Give the position of every Plasmodium parasite.
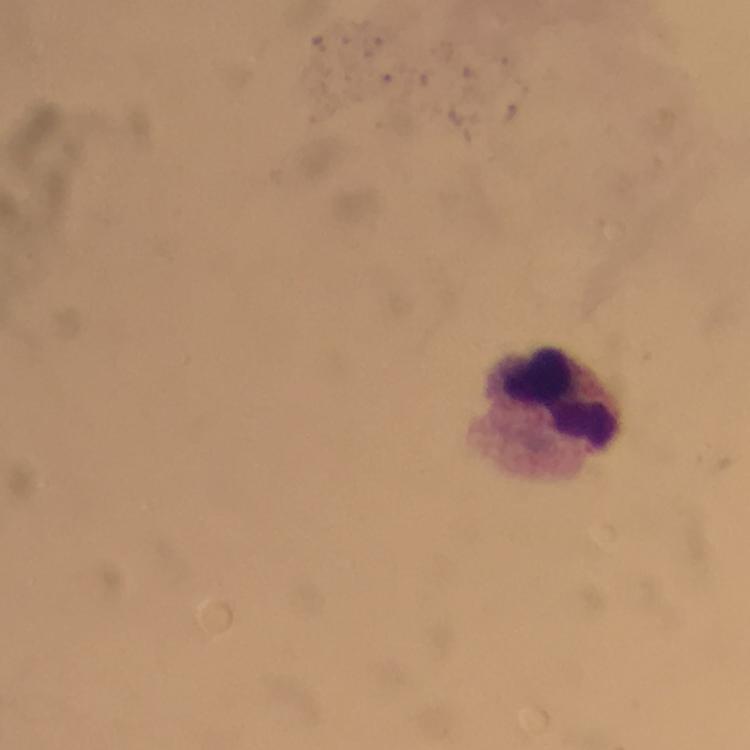
No Plasmodium parasites seen.

image size = 750×750 pixels
cropped from = one field of view
stain = Giemsa
capture = smartphone camera through the microscope
context = from a malaria diagnostic workup
leukocyte locations = approximate centers as {x, y} in pixels: {560, 397}
immersion oil = applied
magnification = 100x
preparation = thick blood film